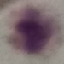 Malaria status: uninfected. Giemsa-stained preparation. Automatically extracted cell patch, resized to 64 × 64 pixels. Acquired by smartphone through the microscope eyepiece. Thin blood film.